Identify the preparation type.
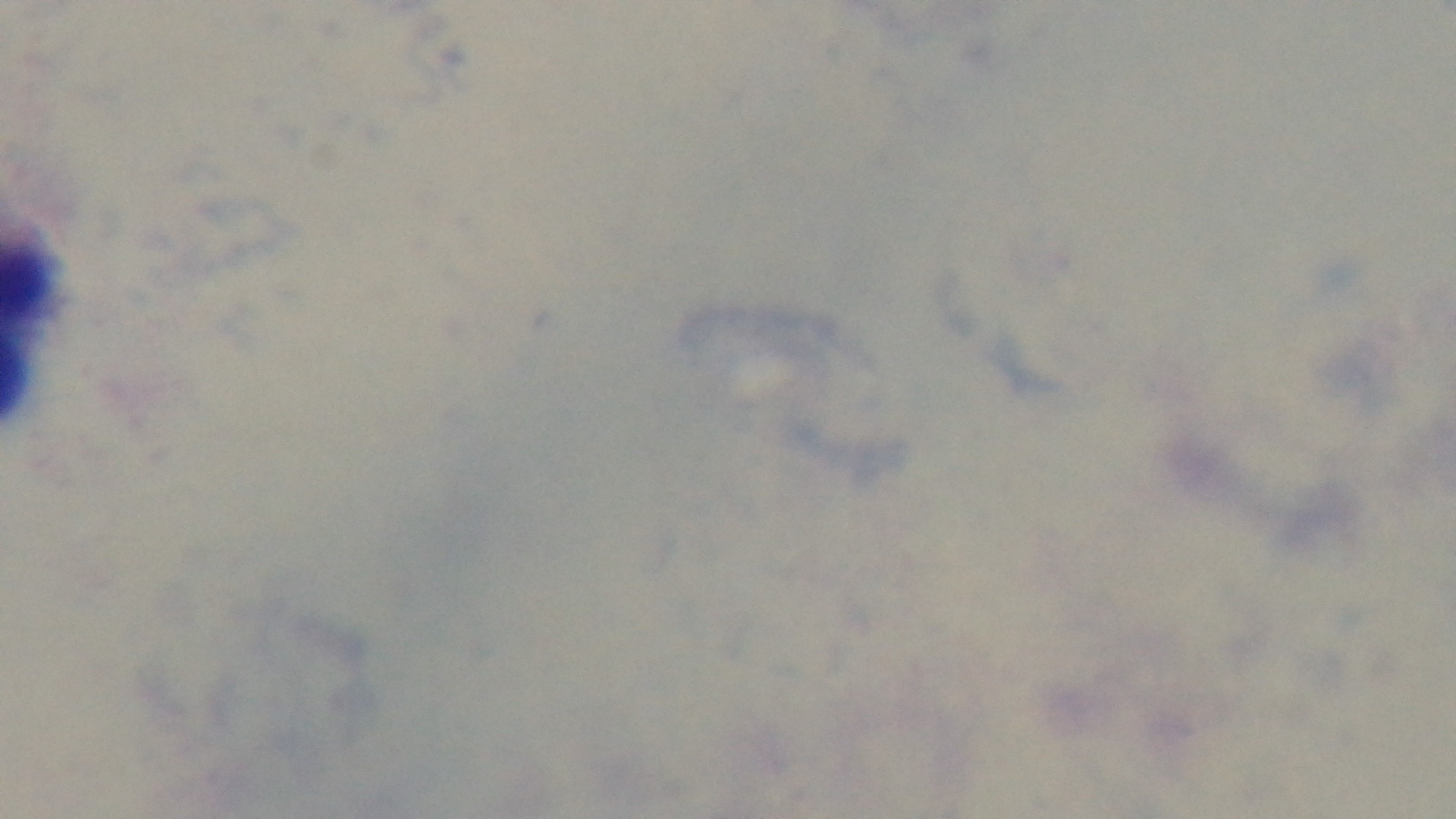
A thick smear.

malaria status = uninfected
stain = Giemsa
capture = mounted 4K digital camera
modality = light microscopy
field of view = one from the slide
objective = 100x oil immersion